Report the malaria status of this cell.
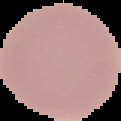

It is uninfected.

From a thin blood smear. Image is 121×121 pixels. The area outside the segmented cell region is set to black.